Identify the blood parasite species.
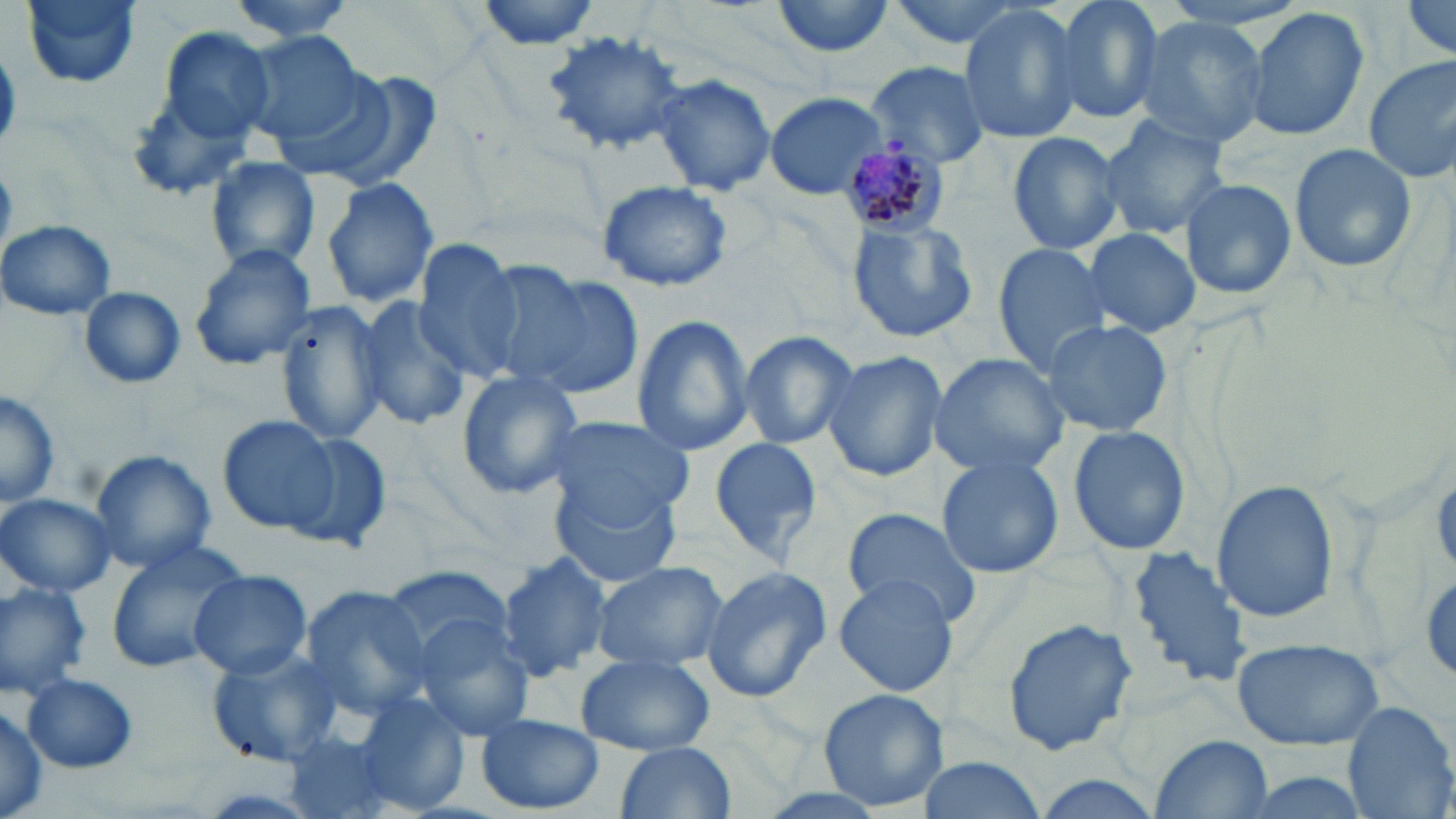

Plasmodium malariae.

Approximate bounding boxes as named x1/y1/x2/y2 corners in pixels. Uninfected red blood cell locations: (x1=20, y1=0, x2=143, y2=89), (x1=226, y1=0, x2=366, y2=42), (x1=473, y1=0, x2=603, y2=48), (x1=770, y1=0, x2=897, y2=59), (x1=882, y1=0, x2=1038, y2=51), (x1=1049, y1=0, x2=1167, y2=125), (x1=1397, y1=1, x2=1454, y2=62), (x1=956, y1=4, x2=1084, y2=144), (x1=1242, y1=5, x2=1371, y2=143), (x1=1130, y1=16, x2=1268, y2=148), (x1=145, y1=25, x2=282, y2=164), (x1=543, y1=28, x2=686, y2=154), (x1=240, y1=31, x2=371, y2=150), (x1=1361, y1=57, x2=1456, y2=185), (x1=868, y1=62, x2=992, y2=166), (x1=304, y1=67, x2=442, y2=191), (x1=650, y1=72, x2=776, y2=198), (x1=764, y1=92, x2=886, y2=199), (x1=1098, y1=114, x2=1232, y2=240), (x1=1006, y1=129, x2=1127, y2=254), (x1=1287, y1=142, x2=1420, y2=275), (x1=203, y1=156, x2=321, y2=274), (x1=320, y1=176, x2=440, y2=309), (x1=1177, y1=177, x2=1297, y2=301), (x1=594, y1=179, x2=736, y2=294), (x1=845, y1=215, x2=980, y2=345), (x1=1, y1=219, x2=117, y2=322), (x1=1081, y1=227, x2=1201, y2=338), (x1=188, y1=243, x2=319, y2=372), (x1=409, y1=245, x2=525, y2=380), (x1=992, y1=245, x2=1117, y2=376), (x1=506, y1=271, x2=643, y2=400), (x1=78, y1=288, x2=186, y2=388), (x1=352, y1=297, x2=472, y2=430), (x1=276, y1=301, x2=394, y2=445), (x1=629, y1=314, x2=756, y2=458), (x1=1039, y1=317, x2=1172, y2=437), (x1=737, y1=330, x2=860, y2=449), (x1=822, y1=352, x2=949, y2=482), (x1=930, y1=354, x2=1068, y2=476), (x1=455, y1=372, x2=586, y2=500), (x1=0, y1=387, x2=59, y2=513), (x1=217, y1=414, x2=338, y2=534), (x1=543, y1=415, x2=695, y2=525), (x1=1067, y1=425, x2=1189, y2=555), (x1=283, y1=431, x2=391, y2=552), (x1=708, y1=436, x2=824, y2=566), (x1=89, y1=449, x2=216, y2=574), (x1=935, y1=456, x2=1063, y2=579), (x1=551, y1=480, x2=683, y2=589), (x1=1211, y1=480, x2=1338, y2=625), (x1=0, y1=493, x2=118, y2=598), (x1=841, y1=508, x2=985, y2=629), (x1=102, y1=540, x2=249, y2=675), (x1=1125, y1=541, x2=1254, y2=691), (x1=495, y1=550, x2=614, y2=682), (x1=590, y1=560, x2=729, y2=674), (x1=386, y1=564, x2=513, y2=660), (x1=698, y1=565, x2=831, y2=701), (x1=188, y1=570, x2=312, y2=679), (x1=833, y1=574, x2=961, y2=699), (x1=0, y1=580, x2=92, y2=698), (x1=298, y1=586, x2=436, y2=718), (x1=409, y1=614, x2=538, y2=742), (x1=1003, y1=615, x2=1138, y2=758), (x1=1229, y1=637, x2=1386, y2=751), (x1=207, y1=647, x2=343, y2=766), (x1=575, y1=653, x2=715, y2=755), (x1=22, y1=673, x2=137, y2=773), (x1=817, y1=688, x2=951, y2=811), (x1=351, y1=691, x2=472, y2=816), (x1=1340, y1=700, x2=1456, y2=819), (x1=0, y1=702, x2=49, y2=818), (x1=476, y1=713, x2=604, y2=814), (x1=1152, y1=733, x2=1273, y2=816), (x1=614, y1=741, x2=737, y2=819), (x1=911, y1=752, x2=1046, y2=819), (x1=1028, y1=770, x2=1169, y2=819), (x1=1226, y1=770, x2=1378, y2=819). Plasmodium malariae-infected red blood cell locations: (x1=840, y1=142, x2=951, y2=239). Captured at 1000x magnification. Image is 1456×819 pixels. Single field of view. Optical microscopy. Thin blood smear. May-Grünwald-Giemsa stain.